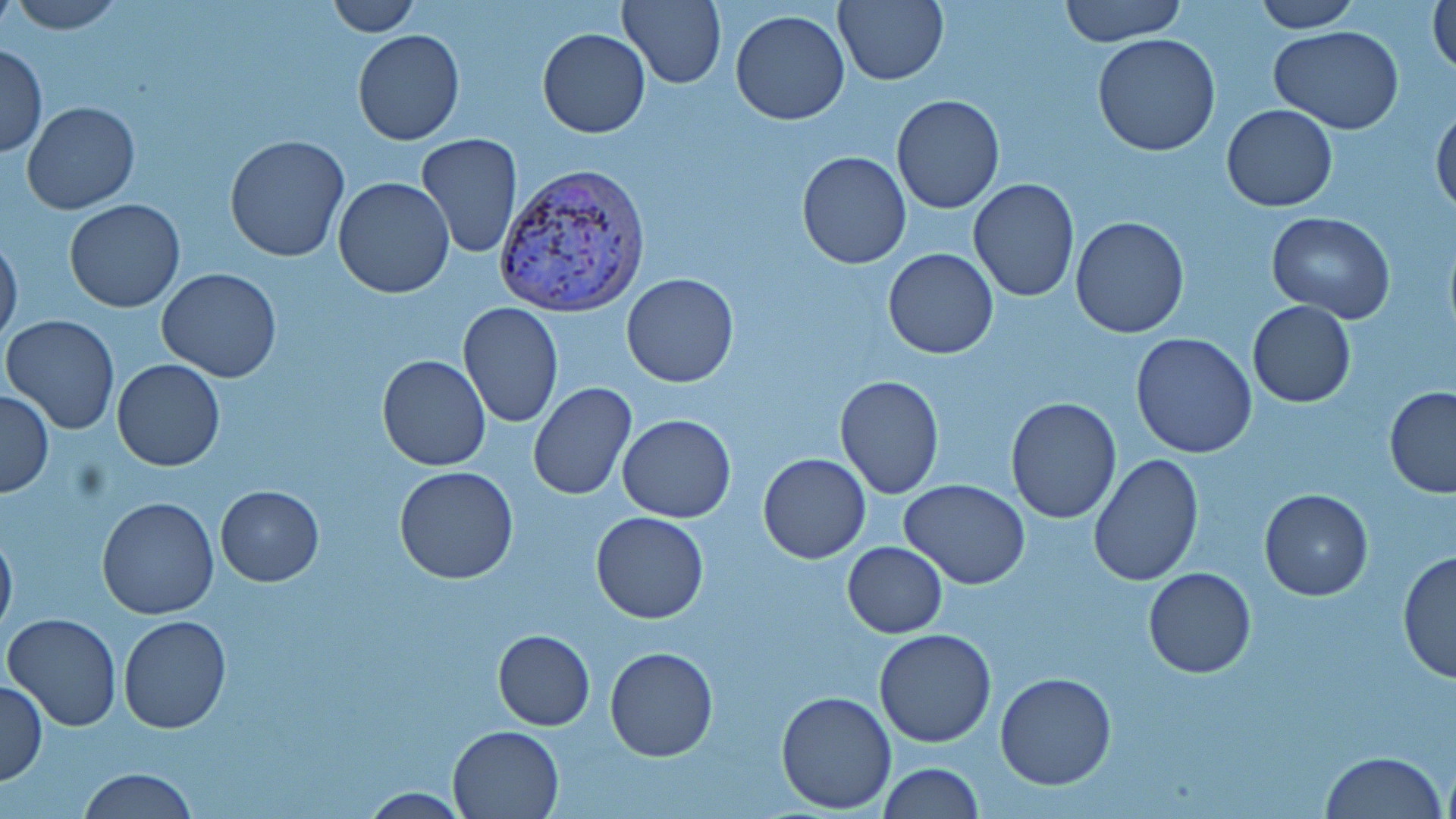

{
  "slide_level_diagnosis": "Plasmodium vivax",
  "modality": "light microscopy",
  "plasmodium_vivax_infected_red_blood_cell_locations": "approximate bounding boxes as (x1,y1)-(x2,y2) corner pairs in pixels: (494,161)-(652,319)",
  "field_of_view": "one of a larger specimen",
  "stain": "May-Grünwald-Giemsa",
  "magnification": "1000x",
  "uninfected_red_blood_cell_locations": "approximate bounding boxes as (x1,y1)-(x2,y2) corner pairs in pixels: (8,0)-(124,32), (324,0)-(420,36), (617,0)-(727,88), (1058,0)-(1186,46), (1428,0)-(1456,80), (832,1)-(949,86), (1254,1)-(1360,31), (731,10)-(850,125), (1270,25)-(1405,132), (537,28)-(650,139), (353,30)-(465,145), (1093,34)-(1221,156), (0,43)-(47,157), (890,94)-(1004,215), (23,102)-(140,215), (1222,105)-(1338,213), (1432,107)-(1456,219), (416,133)-(522,258), (224,134)-(349,262), (797,150)-(911,269), (333,177)-(456,298), (968,177)-(1079,302), (65,199)-(184,313), (1265,211)-(1395,323), (1069,216)-(1190,339), (0,233)-(23,346), (883,248)-(999,360), (156,268)-(283,382), (622,272)-(738,388), (1246,300)-(1356,408), (459,302)-(565,429), (2,314)-(120,434), (1131,333)-(1258,459), (377,354)-(491,471), (111,359)-(225,471), (834,375)-(945,500), (527,382)-(637,501), (1384,387)-(1456,496), (0,389)-(53,496), (1005,397)-(1121,522), (617,414)-(736,523), (758,453)-(870,564), (1089,454)-(1205,586), (394,465)-(521,585), (900,478)-(1030,589), (215,485)-(324,586), (1259,489)-(1372,601), (97,497)-(220,620), (592,511)-(708,624), (0,527)-(17,638), (843,542)-(948,638), (1397,550)-(1455,683), (1143,568)-(1256,678), (5,611)-(122,731), (118,615)-(230,732), (493,628)-(595,730), (875,628)-(998,747), (605,647)-(718,762), (993,674)-(1117,791), (0,679)-(47,786), (774,690)-(897,813), (447,725)-(564,818), (1320,752)-(1445,819), (1440,754)-(1455,819), (878,762)-(983,819), (77,768)-(199,819), (358,787)-(469,817)",
  "preparation": "thin blood smear",
  "image_size": "1456×819 pixels"
}